Locate every blood parasite and identify its species.
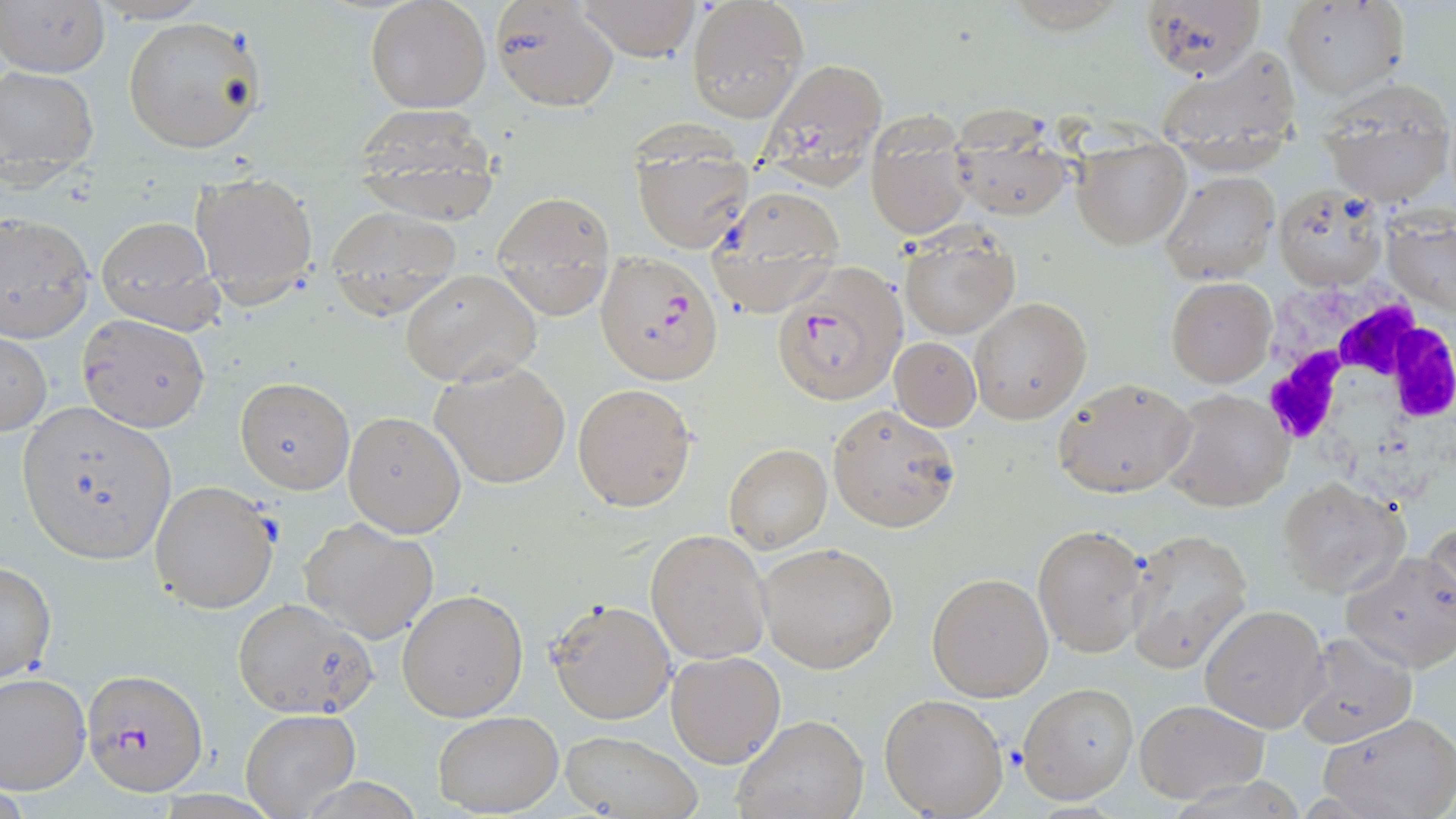
Approximate bounding boxes as named x1/y1/x2/y2 corners in pixels.
Plasmodium falciparum-infected red blood cells: (x1=760, y1=59, x2=885, y2=185), (x1=596, y1=253, x2=725, y2=385), (x1=773, y1=261, x2=906, y2=407), (x1=81, y1=668, x2=208, y2=796).
No Plasmodium ovale, Plasmodium malariae, Plasmodium vivax, Babesia divergens, or Trypanosoma brucei observed.

Summary:
  - White blood cell locations: (x1=1249, y1=274, x2=1456, y2=504)
  - Uninfected red blood cell locations: (x1=1, y1=0, x2=113, y2=78), (x1=365, y1=0, x2=491, y2=114), (x1=489, y1=0, x2=620, y2=112), (x1=576, y1=0, x2=701, y2=60), (x1=1142, y1=0, x2=1267, y2=81), (x1=686, y1=1, x2=807, y2=122), (x1=1282, y1=1, x2=1407, y2=100), (x1=121, y1=16, x2=266, y2=156), (x1=1156, y1=44, x2=1300, y2=147), (x1=0, y1=66, x2=100, y2=185), (x1=1319, y1=84, x2=1455, y2=206), (x1=351, y1=103, x2=500, y2=224), (x1=865, y1=113, x2=971, y2=238), (x1=947, y1=118, x2=1070, y2=221), (x1=631, y1=135, x2=752, y2=252), (x1=1074, y1=141, x2=1190, y2=249), (x1=191, y1=168, x2=320, y2=304), (x1=1160, y1=171, x2=1280, y2=283), (x1=708, y1=186, x2=847, y2=311), (x1=1272, y1=186, x2=1388, y2=290), (x1=491, y1=191, x2=616, y2=315), (x1=324, y1=204, x2=462, y2=313), (x1=0, y1=212, x2=95, y2=345), (x1=93, y1=216, x2=222, y2=331), (x1=899, y1=230, x2=1019, y2=339), (x1=400, y1=268, x2=541, y2=387), (x1=1166, y1=277, x2=1276, y2=388), (x1=970, y1=298, x2=1091, y2=422), (x1=78, y1=312, x2=210, y2=431), (x1=0, y1=332, x2=48, y2=436), (x1=890, y1=337, x2=980, y2=430), (x1=431, y1=358, x2=571, y2=489), (x1=235, y1=377, x2=354, y2=495), (x1=1051, y1=377, x2=1195, y2=498), (x1=572, y1=383, x2=696, y2=512), (x1=1164, y1=390, x2=1293, y2=512), (x1=15, y1=401, x2=176, y2=565), (x1=827, y1=404, x2=961, y2=531), (x1=343, y1=411, x2=464, y2=536), (x1=724, y1=443, x2=832, y2=553), (x1=1275, y1=477, x2=1409, y2=598), (x1=148, y1=479, x2=280, y2=614), (x1=301, y1=517, x2=439, y2=644), (x1=1424, y1=521, x2=1456, y2=632), (x1=1033, y1=524, x2=1146, y2=657), (x1=1125, y1=528, x2=1253, y2=671), (x1=646, y1=529, x2=772, y2=665), (x1=756, y1=542, x2=898, y2=672), (x1=1343, y1=551, x2=1456, y2=674), (x1=0, y1=561, x2=57, y2=685), (x1=927, y1=572, x2=1055, y2=702), (x1=397, y1=588, x2=530, y2=722), (x1=232, y1=597, x2=376, y2=719), (x1=546, y1=597, x2=676, y2=723), (x1=1200, y1=604, x2=1328, y2=733), (x1=1294, y1=633, x2=1417, y2=749), (x1=664, y1=650, x2=786, y2=769), (x1=0, y1=673, x2=92, y2=793), (x1=1019, y1=682, x2=1138, y2=803), (x1=879, y1=693, x2=1007, y2=818), (x1=1133, y1=699, x2=1268, y2=803), (x1=240, y1=709, x2=361, y2=818), (x1=431, y1=711, x2=563, y2=815), (x1=1318, y1=712, x2=1456, y2=819), (x1=731, y1=715, x2=868, y2=819), (x1=560, y1=730, x2=700, y2=818)
  - Slide-level diagnosis: Plasmodium falciparum
  - Stain: May-Grünwald-Giemsa
  - Magnification: 1000x
  - Modality: optical microscopy
  - Image size: 1456×819 pixels
  - Preparation: thin blood smear
  - Field of view: single